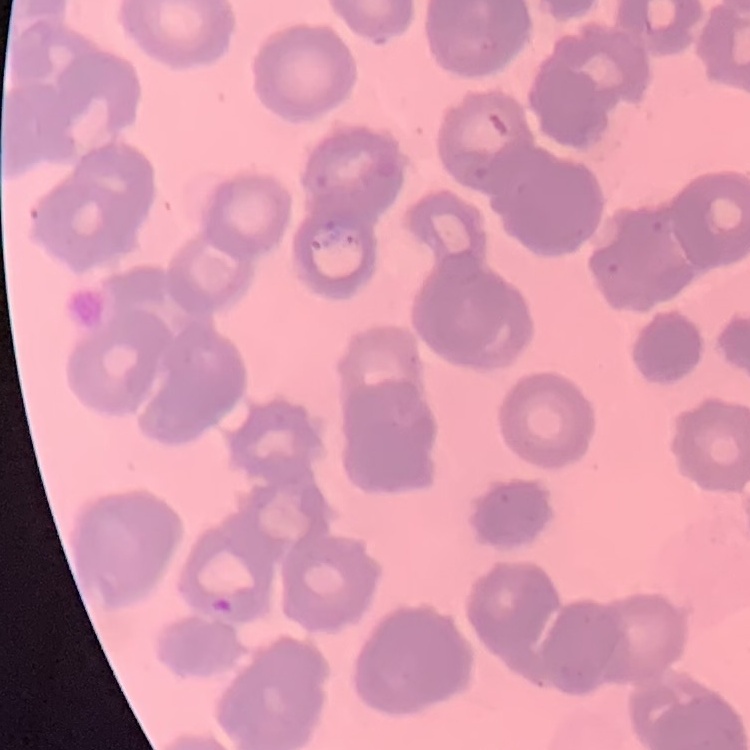
The red blood cells show rouleaux formation. Square crop of a larger photomicrograph. Thin blood smear. Stained with either Field's or Giemsa.